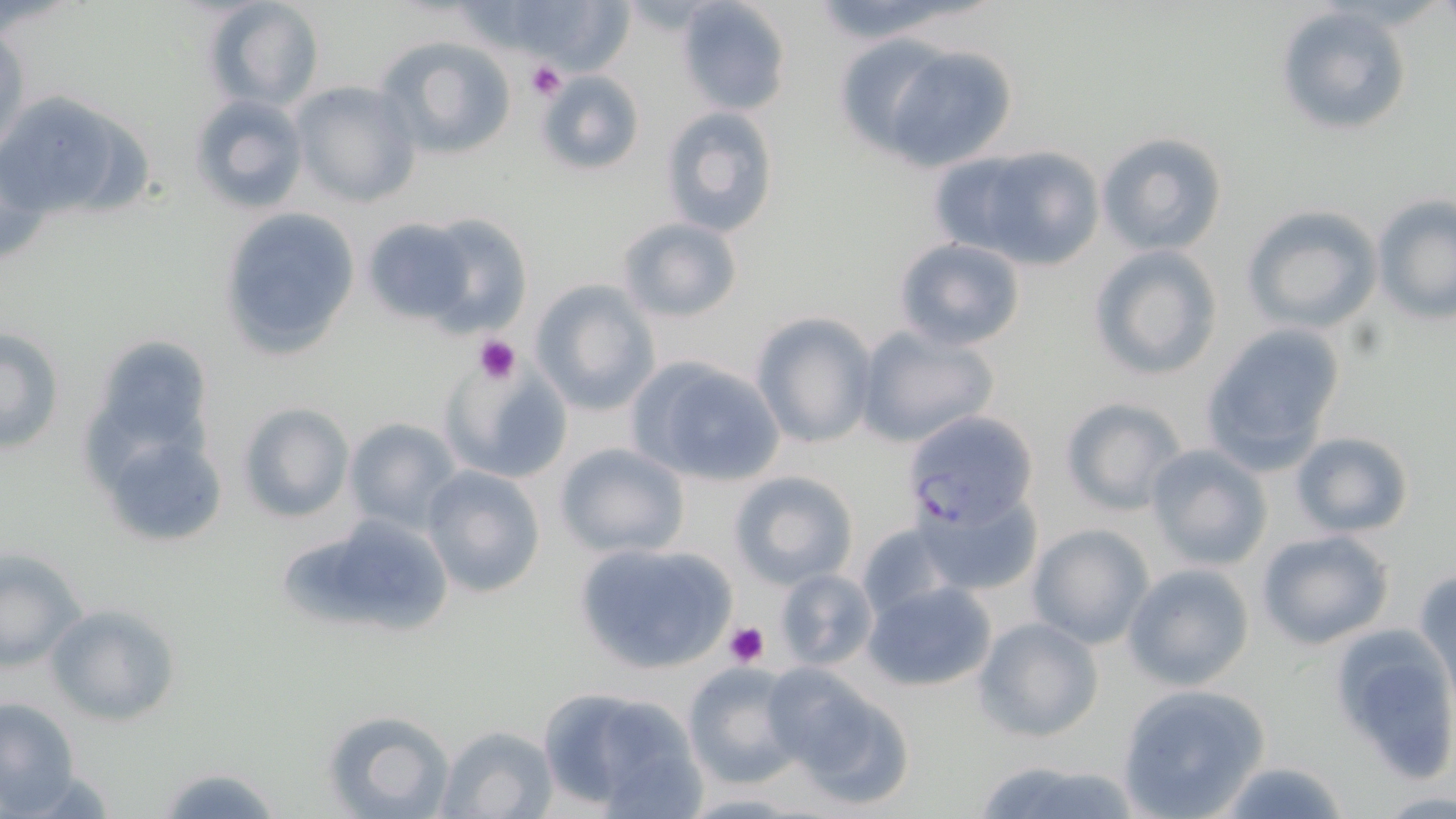
Summary:
  - Coordinate format: approximate bounding boxes as named x1/y1/x2/y2 corners in pixels
  - Uninfected red blood cell locations: (x1=203, y1=0, x2=326, y2=111), (x1=677, y1=0, x2=791, y2=116), (x1=1274, y1=5, x2=1413, y2=138), (x1=1, y1=26, x2=28, y2=155), (x1=376, y1=33, x2=520, y2=160), (x1=878, y1=44, x2=1018, y2=173), (x1=537, y1=71, x2=645, y2=175), (x1=289, y1=82, x2=420, y2=209), (x1=0, y1=90, x2=118, y2=221), (x1=188, y1=93, x2=309, y2=216), (x1=659, y1=106, x2=779, y2=238), (x1=54, y1=108, x2=153, y2=216), (x1=1096, y1=131, x2=1229, y2=257), (x1=947, y1=142, x2=1104, y2=269), (x1=1371, y1=197, x2=1456, y2=323), (x1=218, y1=205, x2=360, y2=361), (x1=1242, y1=205, x2=1383, y2=331), (x1=414, y1=214, x2=533, y2=333), (x1=363, y1=217, x2=478, y2=326), (x1=617, y1=217, x2=742, y2=323), (x1=894, y1=238, x2=1026, y2=351), (x1=1088, y1=245, x2=1223, y2=380), (x1=530, y1=280, x2=660, y2=415), (x1=751, y1=312, x2=879, y2=451), (x1=1199, y1=323, x2=1347, y2=474), (x1=855, y1=324, x2=1000, y2=447), (x1=1, y1=325, x2=64, y2=455), (x1=439, y1=354, x2=575, y2=487), (x1=625, y1=354, x2=788, y2=491), (x1=1059, y1=397, x2=1189, y2=514), (x1=239, y1=403, x2=352, y2=523), (x1=93, y1=411, x2=234, y2=556), (x1=343, y1=417, x2=464, y2=531), (x1=1289, y1=430, x2=1415, y2=538), (x1=554, y1=441, x2=690, y2=557), (x1=1145, y1=444, x2=1273, y2=570), (x1=421, y1=465, x2=546, y2=598), (x1=729, y1=470, x2=857, y2=588), (x1=915, y1=492, x2=1042, y2=597), (x1=280, y1=515, x2=453, y2=640), (x1=856, y1=521, x2=962, y2=624), (x1=1026, y1=523, x2=1155, y2=649), (x1=1255, y1=529, x2=1395, y2=651), (x1=573, y1=540, x2=741, y2=674), (x1=0, y1=549, x2=87, y2=671), (x1=1123, y1=563, x2=1255, y2=691), (x1=774, y1=568, x2=877, y2=669), (x1=1412, y1=569, x2=1456, y2=691), (x1=864, y1=581, x2=997, y2=692), (x1=44, y1=602, x2=182, y2=727), (x1=974, y1=617, x2=1103, y2=743), (x1=1331, y1=627, x2=1456, y2=781), (x1=682, y1=663, x2=804, y2=787), (x1=774, y1=677, x2=916, y2=810), (x1=534, y1=683, x2=705, y2=815), (x1=1115, y1=683, x2=1269, y2=818), (x1=0, y1=697, x2=81, y2=814), (x1=323, y1=708, x2=455, y2=818), (x1=435, y1=724, x2=559, y2=819), (x1=970, y1=760, x2=1146, y2=819), (x1=1211, y1=761, x2=1351, y2=818), (x1=154, y1=764, x2=284, y2=818)
  - Plasmodium falciparum-infected red blood cell locations: (x1=901, y1=410, x2=1039, y2=532)
  - Platelet locations: (x1=525, y1=59, x2=567, y2=101), (x1=472, y1=335, x2=520, y2=383), (x1=723, y1=620, x2=772, y2=667)
  - Slide-level diagnosis: Plasmodium falciparum
  - Stain: May-Grünwald-Giemsa
  - Magnification: 1000x
  - Field of view: one of a larger specimen
  - Modality: optical microscopy
  - Image size: 1456×819 pixels
  - Preparation: thin blood smear